Name the cell type shown.
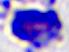
A leukocyte.

Summary:
  - Magnification: 400x
  - Modality: photomicrograph